Comment on the morphology of the erythrocytes.
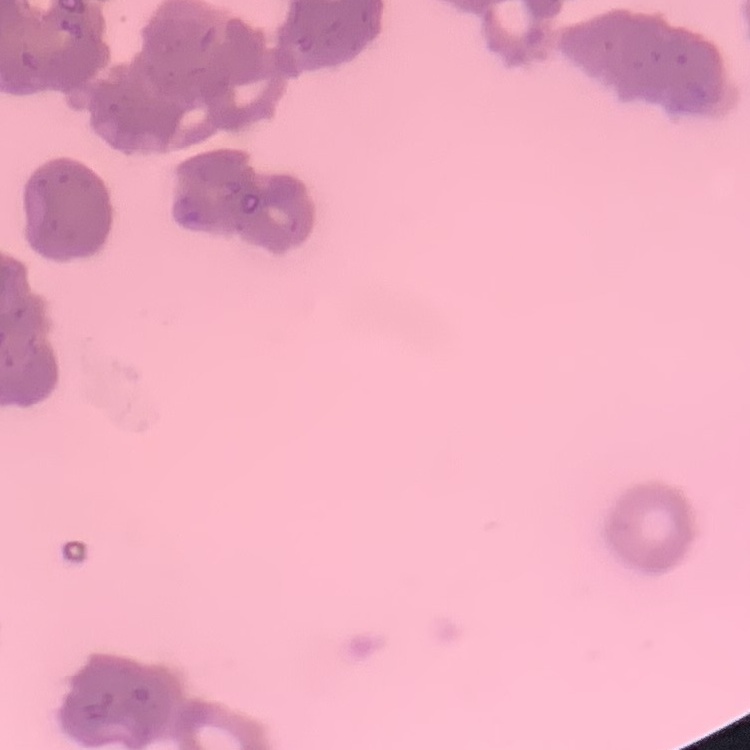
Rouleaux formation.

Thin blood smear. Field's or Giemsa stain. One tile cut from a larger photomicrograph.